Describe the morphology of the red blood cells.
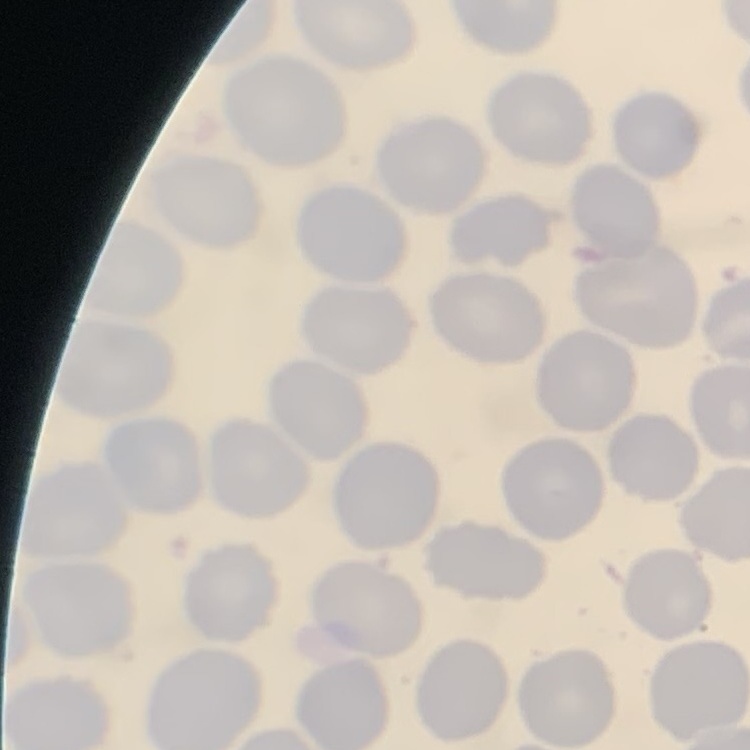

They show no rouleaux formation.

Summary:
  - Preparation: thin blood film
  - Stain: Field's or Giemsa
  - Image type: one tile cut from a larger photomicrograph